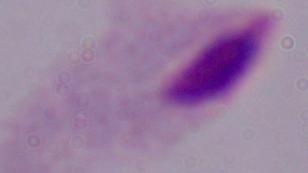
Summary:
  - Magnification: 1000x
  - Modality: photomicrograph
  - Identification: trichomonad